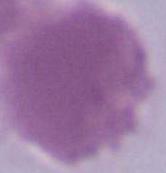
Summary:
  - Magnification: 1000x
  - Modality: micrograph
  - Identification: red blood cell